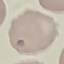

Malaria status: uninfected. Acquired by smartphone through the microscope eyepiece. Thin blood film. Giemsa-stained preparation. Cell patch, automatically extracted from a larger field of view and resized to 64 × 64 pixels.